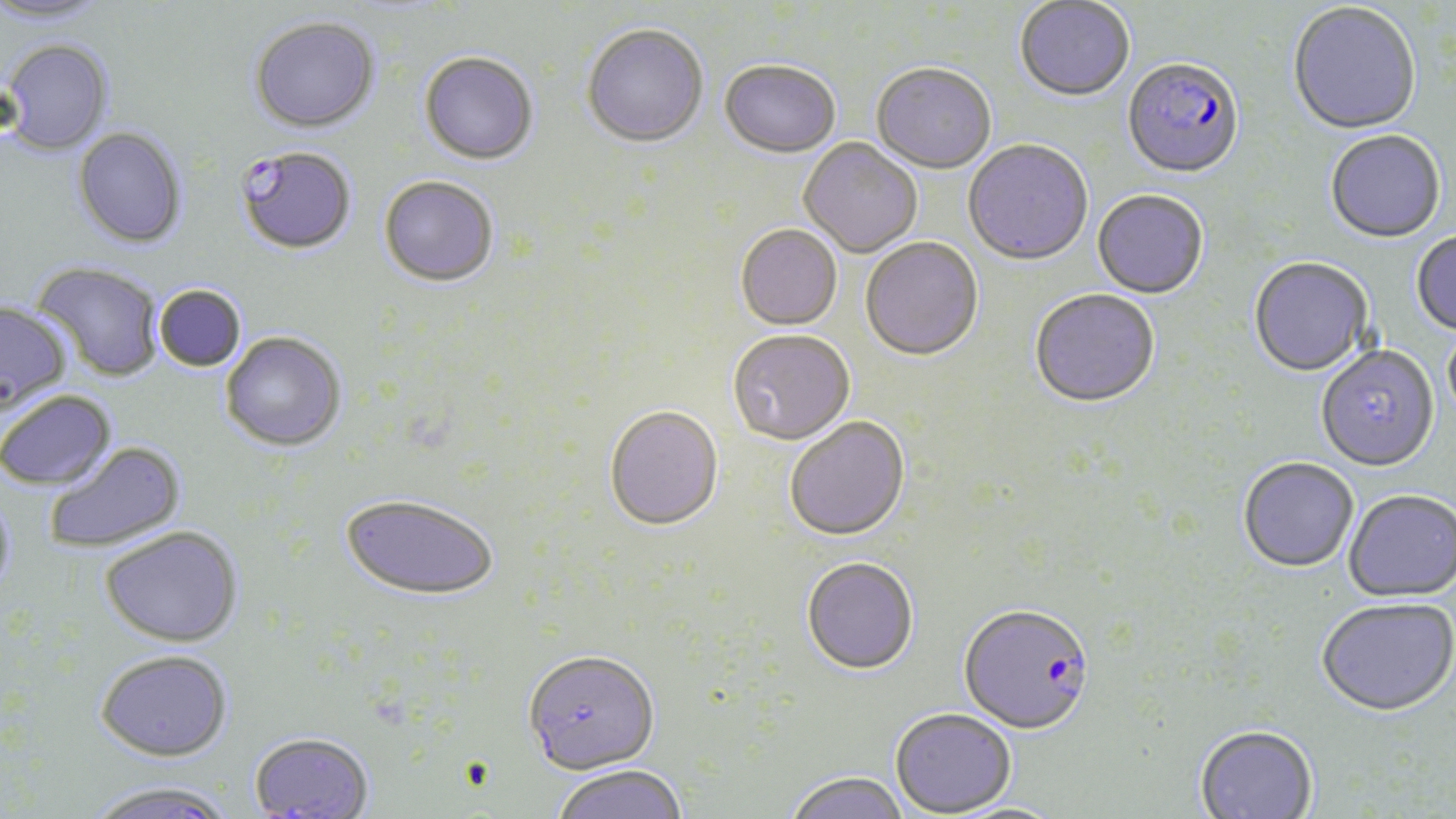 Approximate bounding boxes as (x1, y1, x2, y2) in pixels. Uninfected red blood cell locations: (0, 0, 108, 26), (1014, 1, 1135, 104), (1287, 3, 1421, 137), (248, 16, 380, 134), (582, 27, 708, 150), (2, 39, 114, 155), (419, 54, 538, 166), (719, 62, 840, 160), (871, 65, 996, 176), (73, 127, 188, 248), (1325, 132, 1446, 245), (798, 139, 922, 259), (963, 141, 1093, 268), (378, 177, 499, 289), (1092, 191, 1208, 300), (735, 226, 842, 332), (1411, 233, 1456, 337), (860, 239, 984, 363), (1249, 259, 1373, 379), (32, 261, 164, 382), (154, 285, 247, 372), (1029, 291, 1161, 411), (0, 300, 71, 412), (1443, 323, 1456, 431), (221, 332, 347, 452), (727, 332, 855, 448), (1316, 348, 1440, 474), (0, 390, 116, 491), (604, 408, 723, 533), (785, 419, 910, 543), (43, 441, 185, 554), (1238, 459, 1359, 575), (0, 492, 16, 601), (1343, 492, 1456, 604), (340, 493, 500, 602), (101, 526, 243, 647), (801, 560, 918, 677), (1316, 600, 1456, 720), (95, 649, 234, 762), (523, 652, 660, 778), (890, 710, 1017, 818), (1195, 727, 1318, 819), (248, 732, 375, 818), (552, 765, 688, 819), (784, 773, 910, 819), (84, 781, 240, 819). Plasmodium falciparum-infected red blood cell locations: (1122, 61, 1244, 182), (235, 146, 357, 255), (958, 606, 1095, 738). Slide-level diagnosis: Plasmodium falciparum. May-Grünwald-Giemsa stain. Thin blood smear. Image is 1456×819 pixels. Single field of view. Light microscopy. Captured at 1000x magnification.